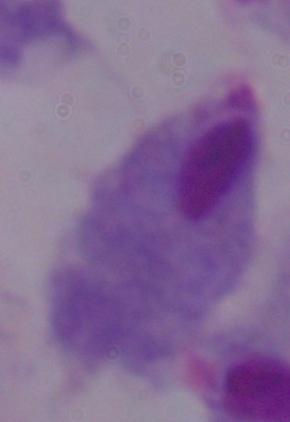 Captured at 1000x magnification. A trichomonad is seen. Photomicrograph.